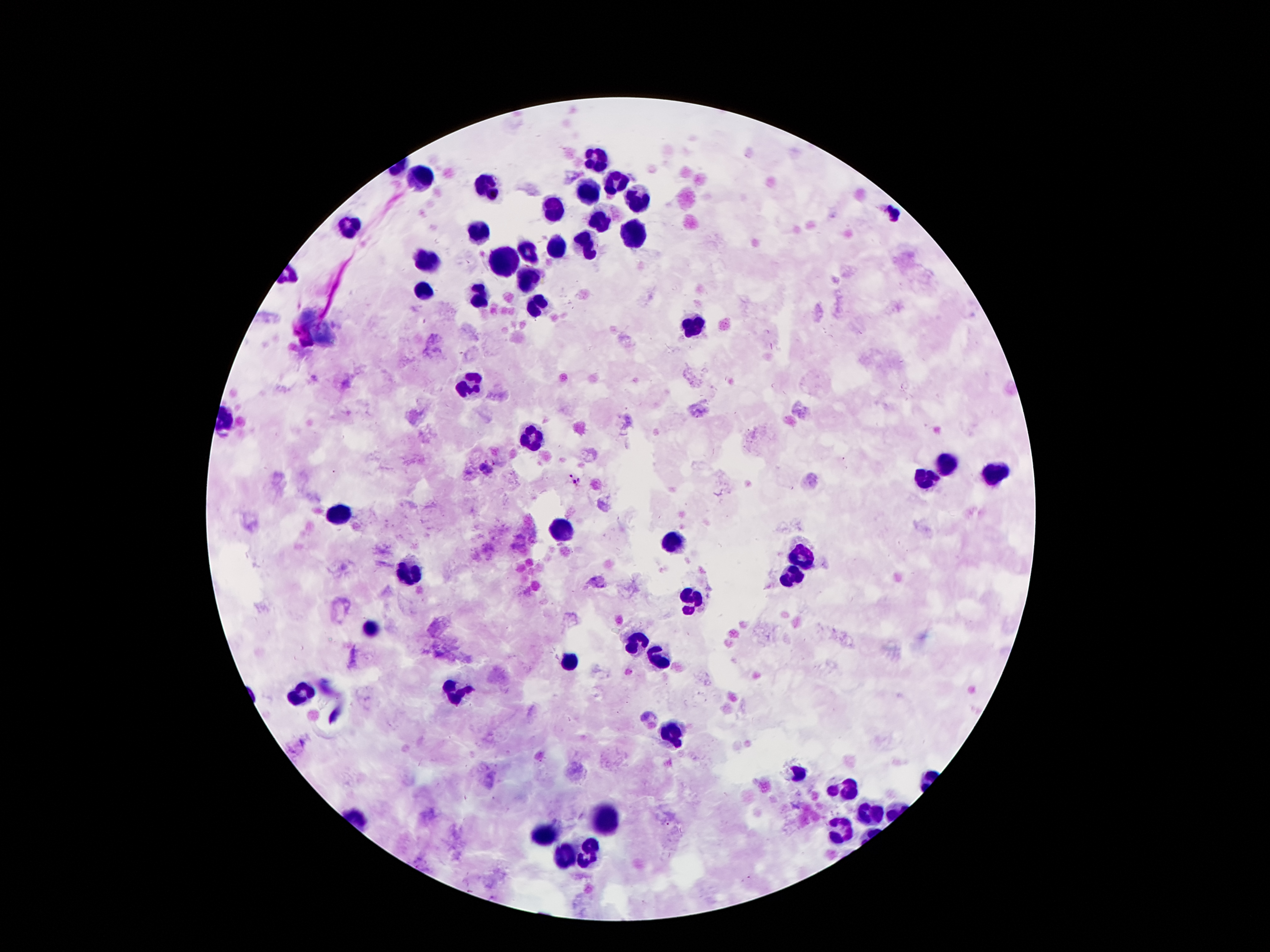
stain: Giemsa
malaria_parasite_locations: 'approximate centers as [x, y] in pixels: [494, 195], [890, 213], [487, 468], [573, 479]'
leukocyte_locations: 'approximate centers as [x, y] in pixels: [596, 157], [421, 179], [484, 185], [611, 185], [591, 190], [637, 198], [553, 210], [598, 220], [348, 229], [477, 235], [634, 237], [585, 243], [555, 248], [525, 249], [509, 255], [425, 261], [529, 280], [423, 291], [481, 299], [533, 304], [307, 319], [692, 327], [326, 330], [469, 388], [533, 439], [946, 467], [996, 473], [927, 479], [335, 513], [561, 528], [675, 541], [798, 554], [404, 577], [789, 579], [692, 602], [372, 631], [633, 642], [658, 656], [568, 663], [456, 695], [301, 696], [671, 732], [797, 772], [843, 788], [868, 812], [603, 821], [843, 829], [538, 835], [587, 856], [568, 858]'
magnification: 100x
field_of_view: single
capture: smartphone camera through the microscope eyepiece
preparation: thick blood film
image_size: 1270×952 pixels
patient_malaria_status: positive for Plasmodium falciparum